Classify this cell by malaria status.
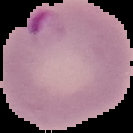
Parasitized.

Image is 133×133 pixels. Segmented cell region on a black background. From a thin blood smear.